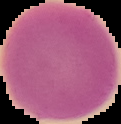 Image is 121×124 pixels. Malaria status: uninfected. From a thin blood smear. The area outside the segmented cell region is set to black.